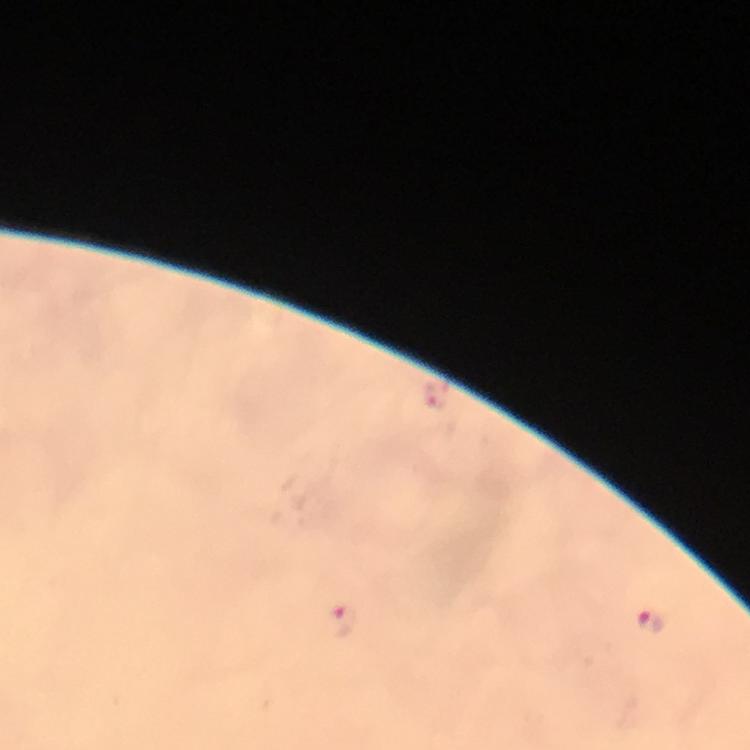
Approximate object centers, in pixels from the top-left corner.
Summary:
  - Malaria parasite locations: (x=435, y=397), (x=340, y=619), (x=651, y=621)
  - Preparation: thick smear
  - Stain: Giemsa
  - Image size: 750×750 pixels
  - Cropped from: one field of view
  - Context: from a malaria diagnostic workup
  - Immersion oil: used
  - Capture: smartphone mounted on the microscope
  - Magnification: 100x